Assess this cell for malaria.
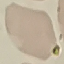

Uninfected.

Summary:
  - Stain: Giemsa
  - Image type: cell patch, automatically extracted from a larger field of view and resized to 64 × 64 pixels
  - Preparation: thin blood smear
  - Capture: smartphone camera at the microscope eyepiece